Locate every Plasmodium parasite.
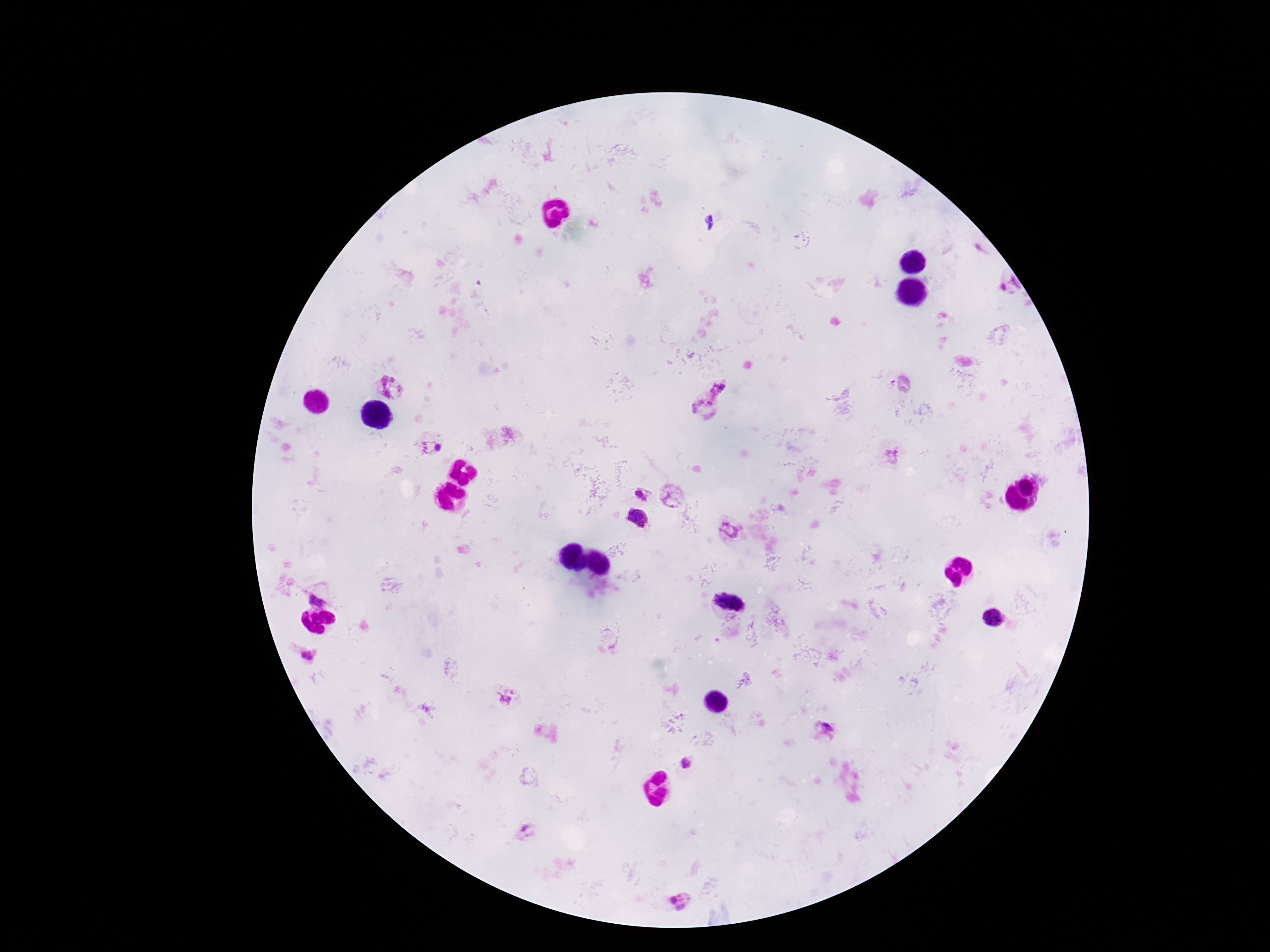
Approximate centers as (x, y) in pixels.
Plasmodium parasites: (711, 222), (393, 385), (719, 387), (702, 408), (431, 448), (892, 455), (642, 495), (671, 499), (637, 517), (729, 529), (319, 593), (728, 599), (306, 656), (507, 696), (826, 731), (688, 762), (526, 830), (679, 901).

patient malaria status = positive
image size = 1270×952 pixels
stain = Giemsa
preparation = thick blood smear
magnification = 100x
capture = smartphone camera through the microscope eyepiece
field of view = one from this slide